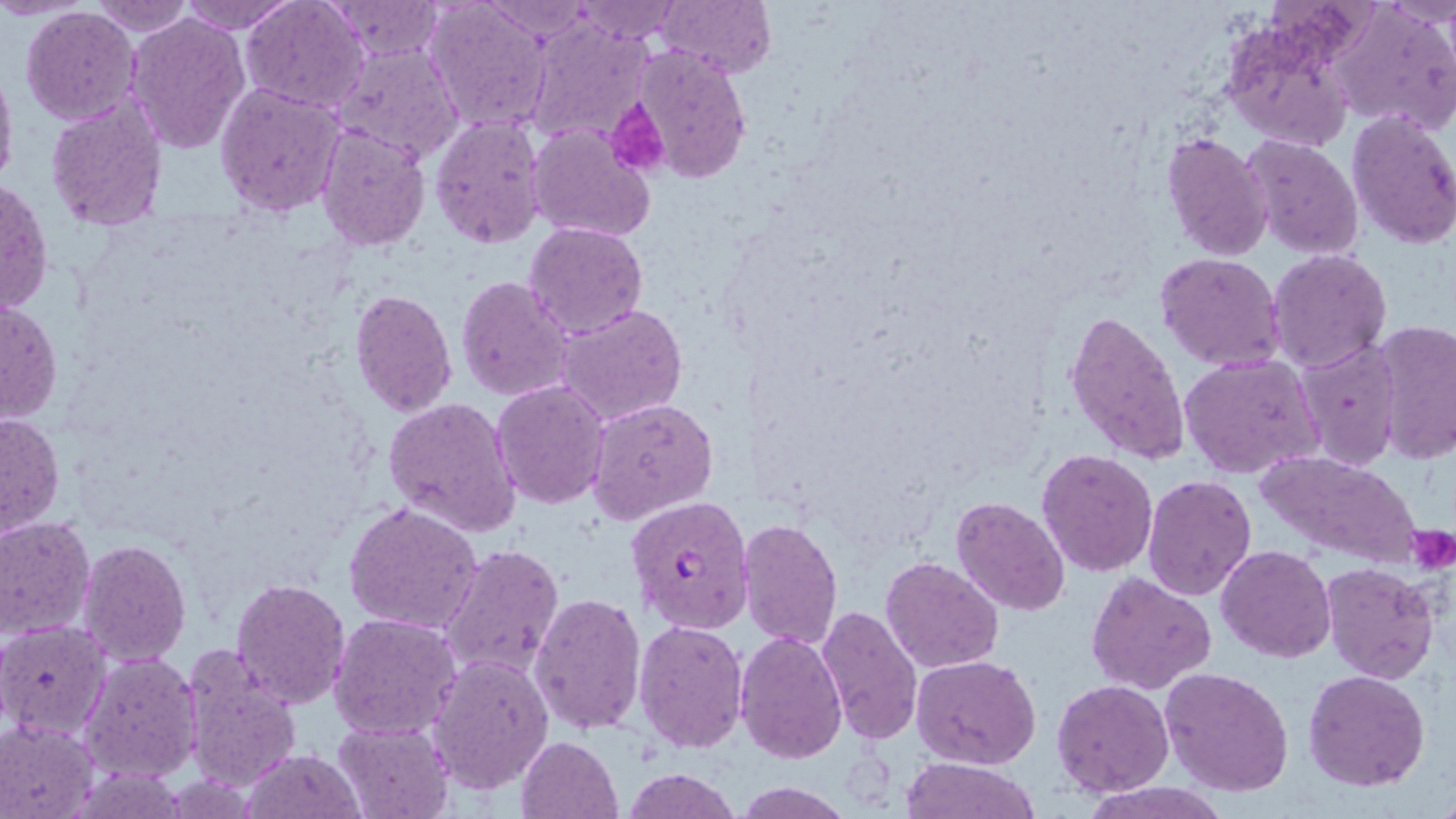
slide-level diagnosis = Plasmodium falciparum
preparation = thin blood film
field of view = one of a larger specimen
magnification = 1000x
stain = May-Grünwald-Giemsa
Plasmodium falciparum-infected red blood cell locations = approximate bounding boxes as [x1, y1, x2, y2] in pixels: [626, 493, 754, 635]
modality = light microscopy
uninfected red blood cell locations = approximate bounding boxes as [x1, y1, x2, y2] in pixels: [87, 0, 199, 37], [176, 0, 297, 34], [324, 0, 445, 61], [424, 0, 554, 132], [572, 0, 682, 44], [660, 0, 775, 76], [242, 1, 369, 113], [1329, 1, 1456, 133], [483, 2, 589, 38], [20, 8, 141, 126], [125, 12, 252, 156], [1219, 12, 1360, 153], [525, 17, 656, 146], [335, 42, 465, 164], [631, 45, 752, 182], [0, 53, 18, 197], [214, 82, 347, 217], [45, 93, 166, 233], [1346, 110, 1456, 251], [429, 113, 547, 250], [527, 123, 656, 243], [316, 125, 431, 250], [1160, 131, 1272, 262], [1242, 135, 1364, 259], [1, 176, 54, 317], [524, 220, 649, 338], [1267, 248, 1394, 374], [1157, 251, 1286, 373], [456, 275, 576, 403], [349, 289, 458, 417], [0, 300, 61, 424], [555, 302, 689, 427], [1063, 307, 1191, 465], [1370, 320, 1456, 465], [1297, 338, 1402, 470], [1178, 354, 1323, 478], [492, 380, 611, 509], [586, 396, 717, 525], [383, 397, 522, 536], [0, 410, 64, 535], [1036, 447, 1159, 577], [1251, 449, 1425, 566], [1141, 476, 1257, 601], [951, 496, 1070, 616], [344, 501, 482, 635], [0, 516, 96, 640], [738, 517, 843, 649], [1410, 523, 1455, 578], [78, 539, 191, 666], [441, 542, 565, 683], [1217, 545, 1336, 663], [880, 556, 1004, 674], [1320, 562, 1439, 685], [1086, 571, 1217, 694], [230, 576, 351, 708], [531, 592, 647, 736], [816, 604, 924, 744], [327, 613, 462, 742], [633, 619, 748, 754], [0, 621, 112, 741], [736, 629, 847, 763], [179, 645, 302, 794], [78, 651, 203, 785], [426, 653, 554, 796], [911, 655, 1041, 770], [1161, 667, 1295, 795], [1303, 669, 1432, 791], [1051, 680, 1174, 796], [1, 719, 99, 819], [331, 720, 455, 818], [516, 735, 622, 819], [241, 747, 362, 818], [902, 757, 1042, 818], [620, 767, 740, 819], [732, 782, 853, 818], [1082, 782, 1228, 819]
image size = 1456×819 pixels
platelet locations = approximate bounding boxes as [x1, y1, x2, y2] in pixels: [605, 99, 669, 180], [1409, 525, 1454, 575]